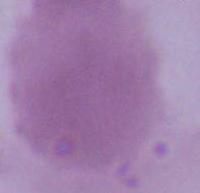
magnification = 1000x
modality = micrograph
identification = red blood cell